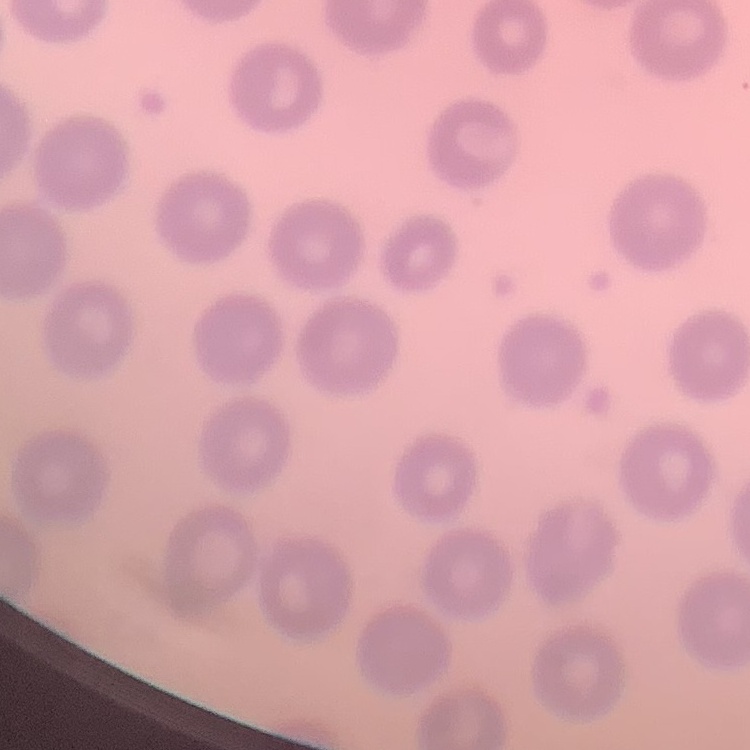

red blood cell morphology = no rouleaux formation
image type = square crop of a larger photomicrograph
preparation = thin blood film
stain = Field's or Giemsa